Report the malaria status of this cell.
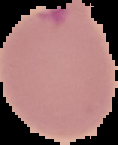

Uninfected.

Summary:
  - Image type: segmented cell region on a black background
  - Image size: 118×145 pixels
  - Preparation: thin blood smear